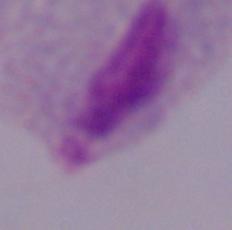

Summary:
  - Magnification: 1000x
  - Modality: micrograph
  - Identification: trichomonad